Outline each uninfected red blood cell.
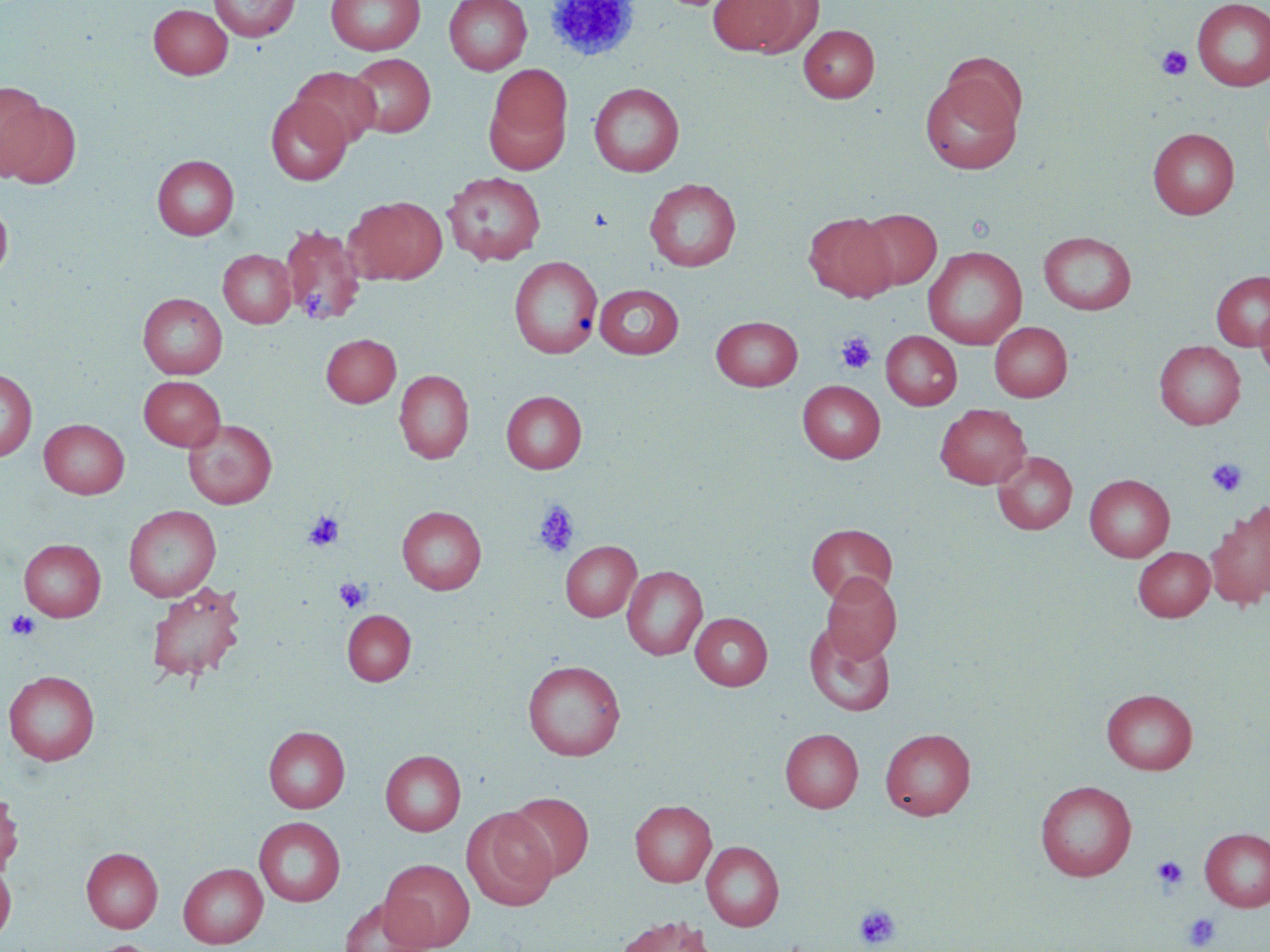

Approximate bounding boxes as (x1,y1)-(x2,y2) corner pairs in pixels.
Uninfected red blood cells: (209,0)-(299,42), (325,0)-(425,55), (443,0)-(532,75), (707,0)-(809,56), (1192,1)-(1270,91), (148,4)-(233,79), (799,24)-(879,102), (347,53)-(435,137), (486,64)-(573,170), (290,66)-(381,148), (919,69)-(1024,175), (0,81)-(48,179), (589,82)-(684,177), (266,96)-(352,184), (2,100)-(82,189), (1148,127)-(1239,218), (152,155)-(239,240), (443,171)-(546,265), (644,178)-(742,271), (345,195)-(447,285), (0,199)-(13,283), (858,208)-(942,290), (804,211)-(897,302), (279,223)-(367,327), (1038,231)-(1137,315), (923,246)-(1027,349), (218,249)-(296,328), (509,256)-(602,358), (1211,270)-(1270,350), (594,284)-(684,358), (138,293)-(227,379), (1255,304)-(1270,380), (712,315)-(803,390), (990,322)-(1072,401), (880,330)-(962,410), (322,334)-(401,407), (1154,340)-(1246,430), (0,369)-(37,463), (394,369)-(474,464), (139,375)-(225,451), (798,380)-(885,462), (501,390)-(587,473), (935,404)-(1032,489), (39,419)-(129,498), (183,419)-(277,509), (992,451)-(1078,535), (1084,474)-(1175,562), (1205,504)-(1270,609), (123,505)-(221,601), (397,506)-(487,594), (806,523)-(897,604), (19,538)-(106,621), (560,541)-(641,621), (1133,546)-(1215,621), (622,565)-(707,660), (821,573)-(900,663), (145,581)-(247,683), (342,610)-(416,686), (690,612)-(773,690), (803,623)-(896,716), (523,660)-(625,761), (4,670)-(100,765), (1101,688)-(1198,774), (264,726)-(350,813), (780,728)-(863,812), (879,728)-(975,820), (380,750)-(466,836), (1035,779)-(1136,881), (0,789)-(23,876), (504,792)-(594,882), (630,799)-(716,886), (462,808)-(558,911), (254,816)-(346,907), (1199,827)-(1270,911), (701,840)-(784,930), (81,847)-(163,932), (379,858)-(475,950), (0,861)-(16,943), (178,863)-(268,948), (339,896)-(437,952), (614,916)-(717,952), (86,940)-(166,952).

slide_level_diagnosis: negative for blood parasites
modality: light microscopy
platelet_locations: 'approximate bounding boxes as (x1,y1)-(x2,y2) corner pairs in pixels: (1156,45)-(1193,81), (302,285)-(337,324), (836,332)-(876,375), (1207,458)-(1247,498), (532,499)-(580,559), (303,511)-(344,551), (334,578)-(369,613), (6,609)-(40,640), (1151,855)-(1188,893), (853,903)-(901,950), (1183,912)-(1220,950)'
image_size: 1270×952 pixels
field_of_view: one of a larger specimen
magnification: 1000x
preparation: thin blood film
stain: May-Grünwald-Giemsa